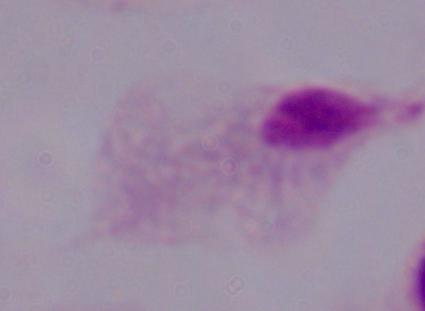

identification = trichomonad
magnification = 1000x
modality = micrograph